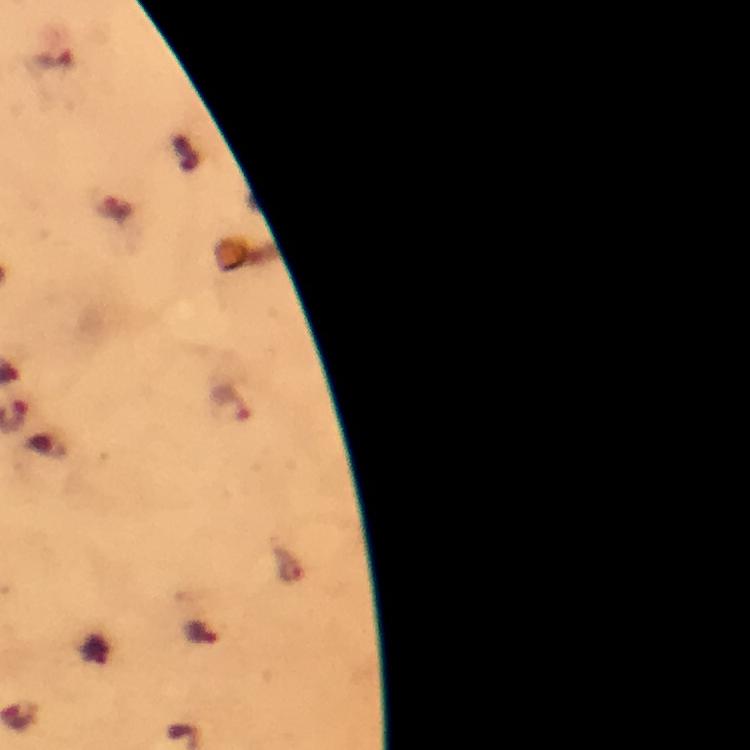
Approximate object centers, in pixels from the top-left corner.
Summary:
  - Malaria parasite locations: (x=233, y=405)
  - Context: from a diagnostic examination for malaria
  - Capture: smartphone camera through the microscope
  - Preparation: thick smear
  - Stain: Giemsa
  - Magnification: 100x
  - Cropped from: a single field of view
  - Image size: 750×750 pixels
  - Immersion oil: applied